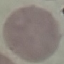
Summary:
  - Result: negative for malaria parasites
  - Image type: automatically extracted cell patch, resized to 64 × 64 pixels
  - Preparation: thin smear
  - Stain: Giemsa
  - Capture: smartphone camera at the microscope eyepiece